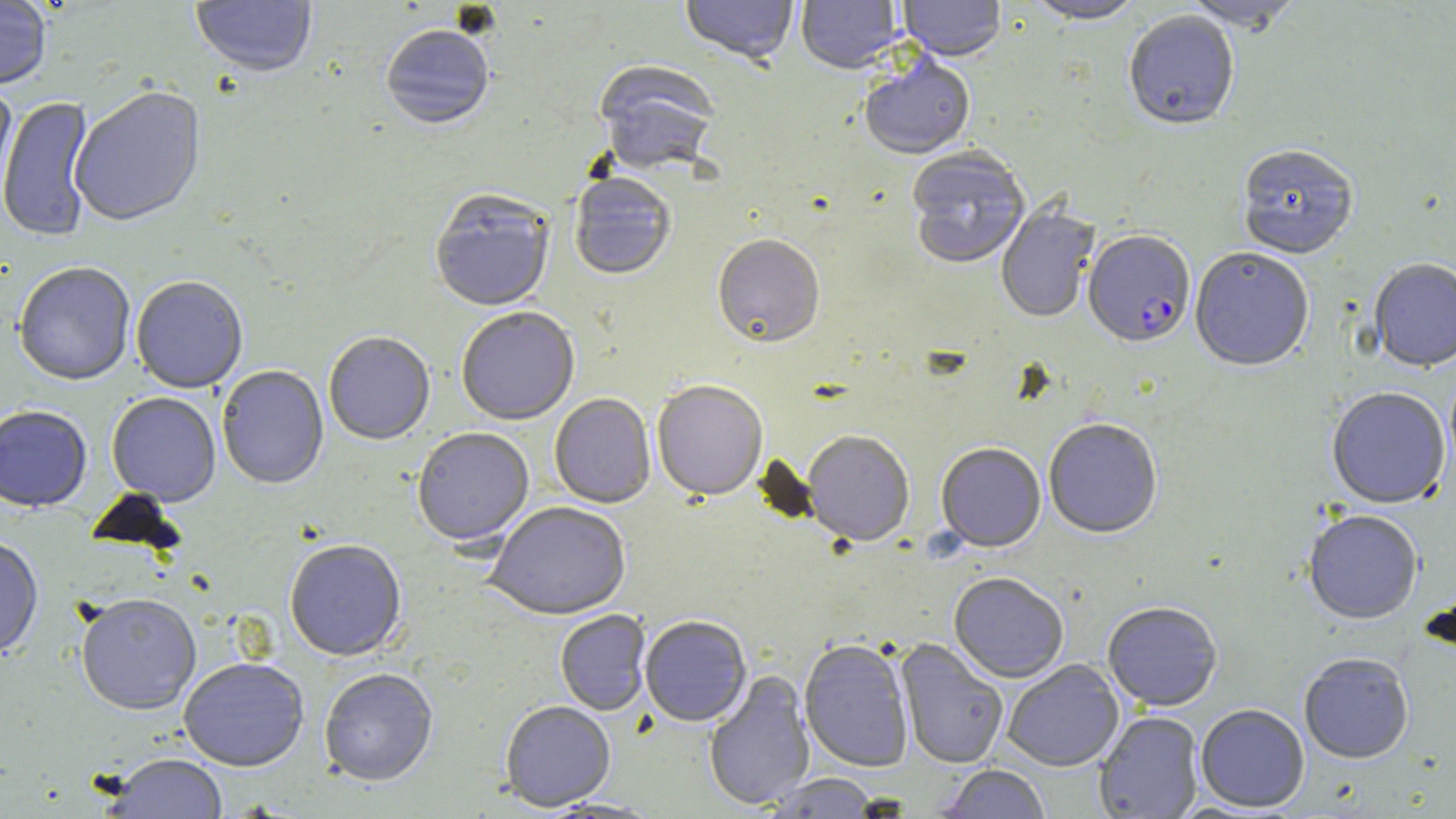 Approximate bounding boxes as (x1,y1)-(x2,y2) corner pairs in pixels. Uninfected red blood cell locations: (190,0)-(317,81), (680,0)-(798,67), (796,0)-(903,75), (898,0)-(1007,63), (1024,0)-(1146,25), (1180,0)-(1306,35), (0,1)-(52,92), (1122,13)-(1240,132), (381,27)-(494,132), (859,57)-(975,161), (593,61)-(721,176), (0,84)-(17,217), (69,87)-(207,229), (0,95)-(96,244), (1236,145)-(1359,259), (906,149)-(1031,270), (569,174)-(676,282), (429,192)-(555,313), (996,202)-(1100,324), (713,236)-(825,349), (1190,247)-(1314,372), (1369,258)-(1456,373), (14,264)-(136,387), (131,277)-(248,395), (456,308)-(580,426), (324,333)-(435,446), (216,366)-(329,490), (652,382)-(768,502), (1326,387)-(1451,510), (107,393)-(221,507), (549,394)-(656,509), (0,407)-(92,514), (1043,418)-(1163,539), (412,428)-(534,548), (803,431)-(914,546), (936,443)-(1046,552), (485,502)-(631,620), (1302,510)-(1423,626), (0,538)-(43,663), (284,541)-(407,663), (949,572)-(1069,684), (75,597)-(202,718), (1102,602)-(1223,712), (555,611)-(652,716), (640,615)-(752,727), (799,639)-(914,773), (895,639)-(1008,769), (1299,654)-(1415,764), (179,659)-(309,773), (1003,660)-(1124,772), (319,669)-(439,787), (703,671)-(816,811), (500,702)-(616,812), (1196,705)-(1309,813), (1094,712)-(1203,818), (107,756)-(229,818), (938,765)-(1051,818), (764,773)-(882,817). Plasmodium falciparum-infected red blood cell locations: (1084,231)-(1195,348). Slide-level diagnosis: Plasmodium falciparum. 1000x magnification. Image is 1456×819 pixels. Thin blood smear. One field of a larger specimen. Optical microscopy. May-Grünwald-Giemsa stain.